Assess this cell for malaria.
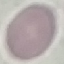

It is uninfected.

stain = Giemsa
image type = cell patch, automatically extracted from a larger field of view and resized to 64 × 64 pixels
preparation = thin blood film
capture = smartphone camera at the microscope eyepiece